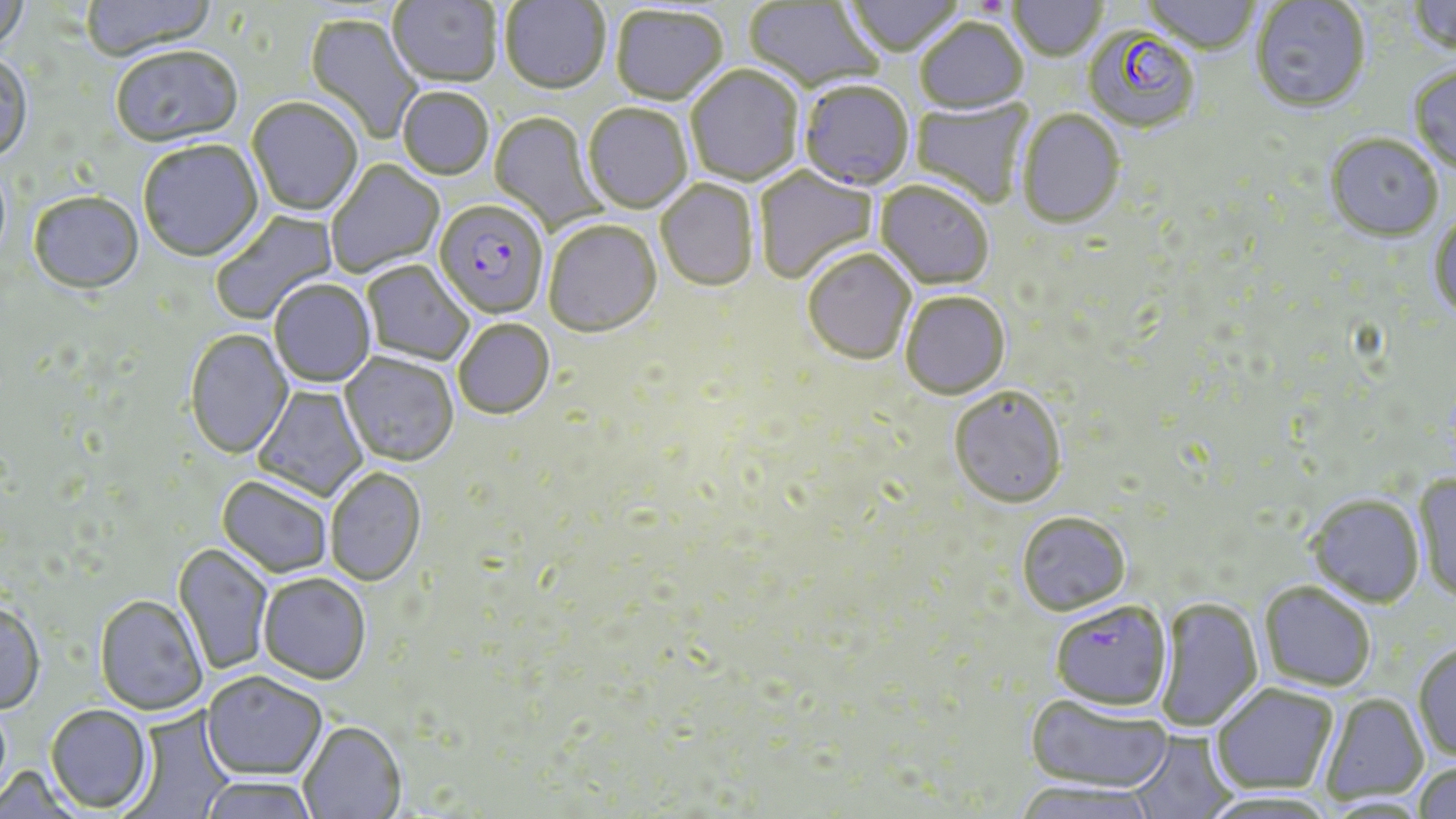
slide_level_diagnosis: Plasmodium falciparum
platelet_locations: 'approximate bounding boxes as [x1, y1, x2, y2] in pixels: [980, 0, 1006, 14]'
magnification: 1000x
stain: May-Grünwald-Giemsa
plasmodium_falciparum_infected_red_blood_cell_locations: 'approximate bounding boxes as [x1, y1, x2, y2] in pixels: [799, 83, 914, 192], [433, 202, 549, 321], [1049, 603, 1172, 713]'
preparation: thin blood film
field_of_view: one of a larger specimen
modality: optical microscopy
image_size: 1456×819 pixels
uninfected_red_blood_cell_locations: 'approximate bounding boxes as [x1, y1, x2, y2] in pixels: [0, 0, 29, 59], [81, 0, 218, 63], [387, 0, 502, 90], [500, 0, 610, 97], [846, 0, 964, 59], [1143, 0, 1260, 56], [1407, 0, 1456, 60], [744, 1, 884, 95], [1008, 1, 1107, 63], [1250, 1, 1371, 114], [610, 7, 728, 108], [303, 13, 423, 145], [916, 21, 1028, 117], [1083, 27, 1201, 135], [111, 48, 243, 149], [0, 56, 33, 166], [685, 66, 804, 188], [1409, 67, 1456, 176], [397, 89, 494, 181], [911, 96, 1035, 208], [247, 99, 363, 218], [584, 105, 693, 215], [1017, 110, 1125, 231], [489, 112, 606, 232], [1325, 135, 1443, 244], [138, 141, 264, 264], [326, 160, 444, 278], [754, 167, 878, 285], [656, 181, 758, 293], [874, 182, 994, 292], [29, 195, 144, 296], [211, 208, 339, 325], [1428, 215, 1456, 320], [544, 221, 662, 340], [802, 250, 916, 367], [362, 262, 474, 366], [270, 281, 376, 388], [900, 293, 1011, 401], [454, 321, 555, 421], [185, 330, 293, 461], [339, 354, 459, 468], [252, 385, 368, 501], [949, 389, 1067, 511], [325, 469, 426, 588], [1413, 475, 1456, 607], [216, 477, 333, 579], [1307, 496, 1425, 608], [1016, 514, 1131, 617], [172, 544, 273, 676], [259, 575, 371, 686], [1258, 583, 1376, 693], [94, 597, 207, 716], [1155, 598, 1264, 732], [0, 602, 45, 715], [1413, 643, 1456, 763], [202, 673, 327, 782], [1210, 685, 1339, 796], [1319, 693, 1429, 805], [1025, 694, 1172, 795], [45, 705, 154, 814], [121, 707, 236, 819], [299, 723, 407, 819], [1129, 731, 1239, 819], [1413, 762, 1456, 819], [198, 777, 320, 819], [1010, 782, 1159, 819], [1195, 790, 1340, 819]'